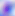
Summary:
  - Identification: Toxoplasma gondii
  - Magnification: 400x
  - Modality: micrograph